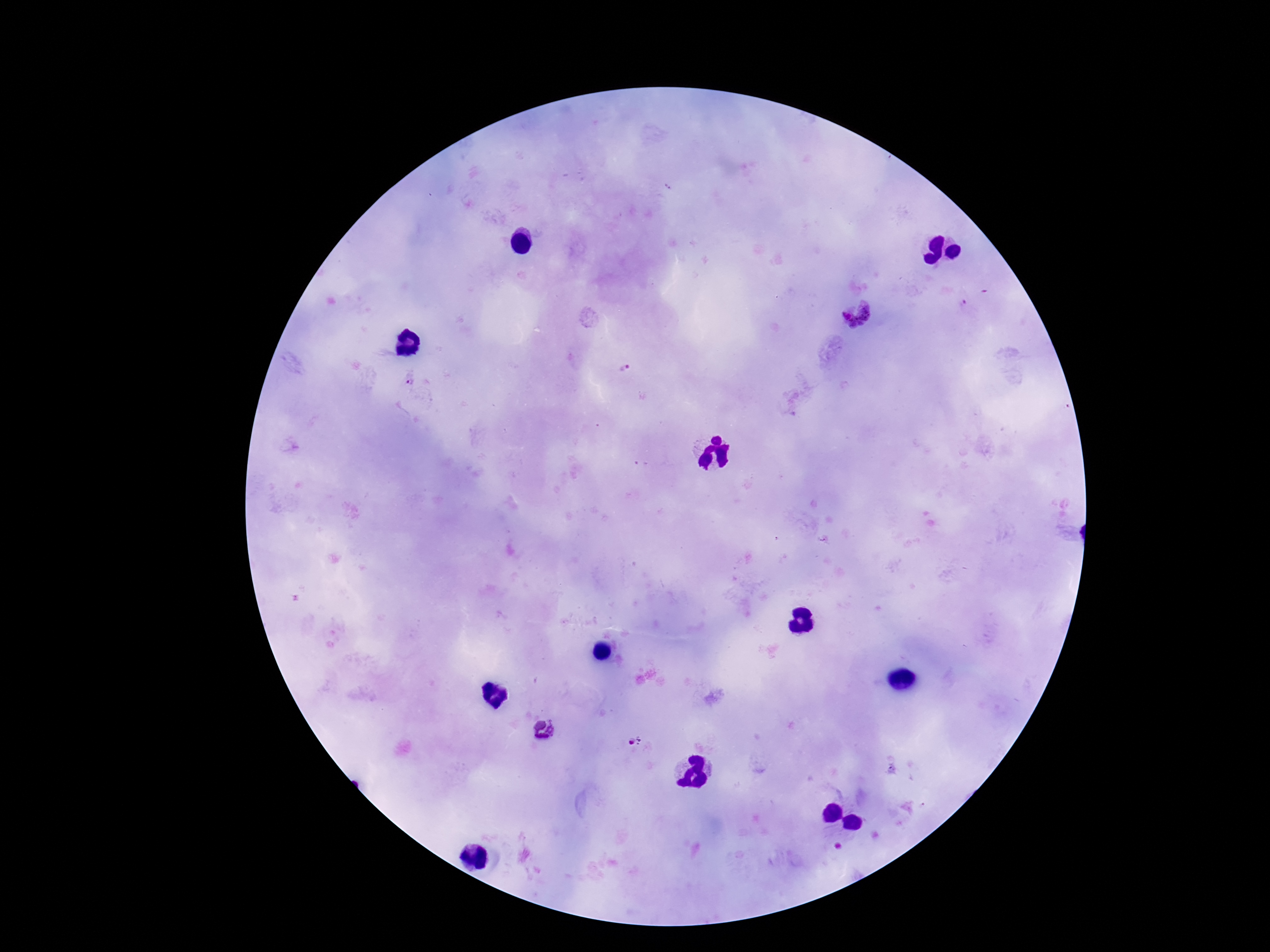
Approximate centers as {x, y} in pixels.
Summary:
  - Plasmodium parasite locations: {855, 311}, {626, 370}, {409, 381}, {543, 730}, {635, 740}
  - Capture: smartphone camera through the microscope eyepiece
  - Stain: Giemsa
  - Magnification: 100x
  - Image size: 1270×952 pixels
  - Patient malaria status: positive
  - Field of view: single
  - Preparation: thick peripheral-blood smear